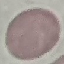

Summary:
  - Result: negative for malaria parasites
  - Image type: cell patch, automatically extracted from a larger field of view and resized to 64 × 64 pixels
  - Stain: Giemsa
  - Preparation: thin blood smear
  - Capture: smartphone through the microscope eyepiece